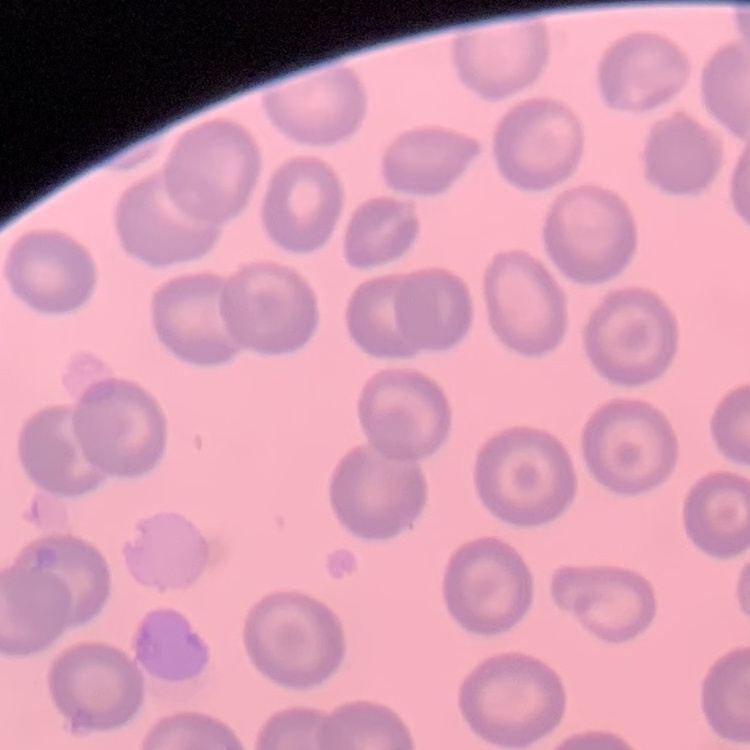

Summary:
  - Red blood cell morphology: no rouleaux formation
  - Image type: one tile cut from a larger photomicrograph
  - Preparation: thin blood film
  - Stain: Field's or Giemsa